Point out each Plasmodium parasite.
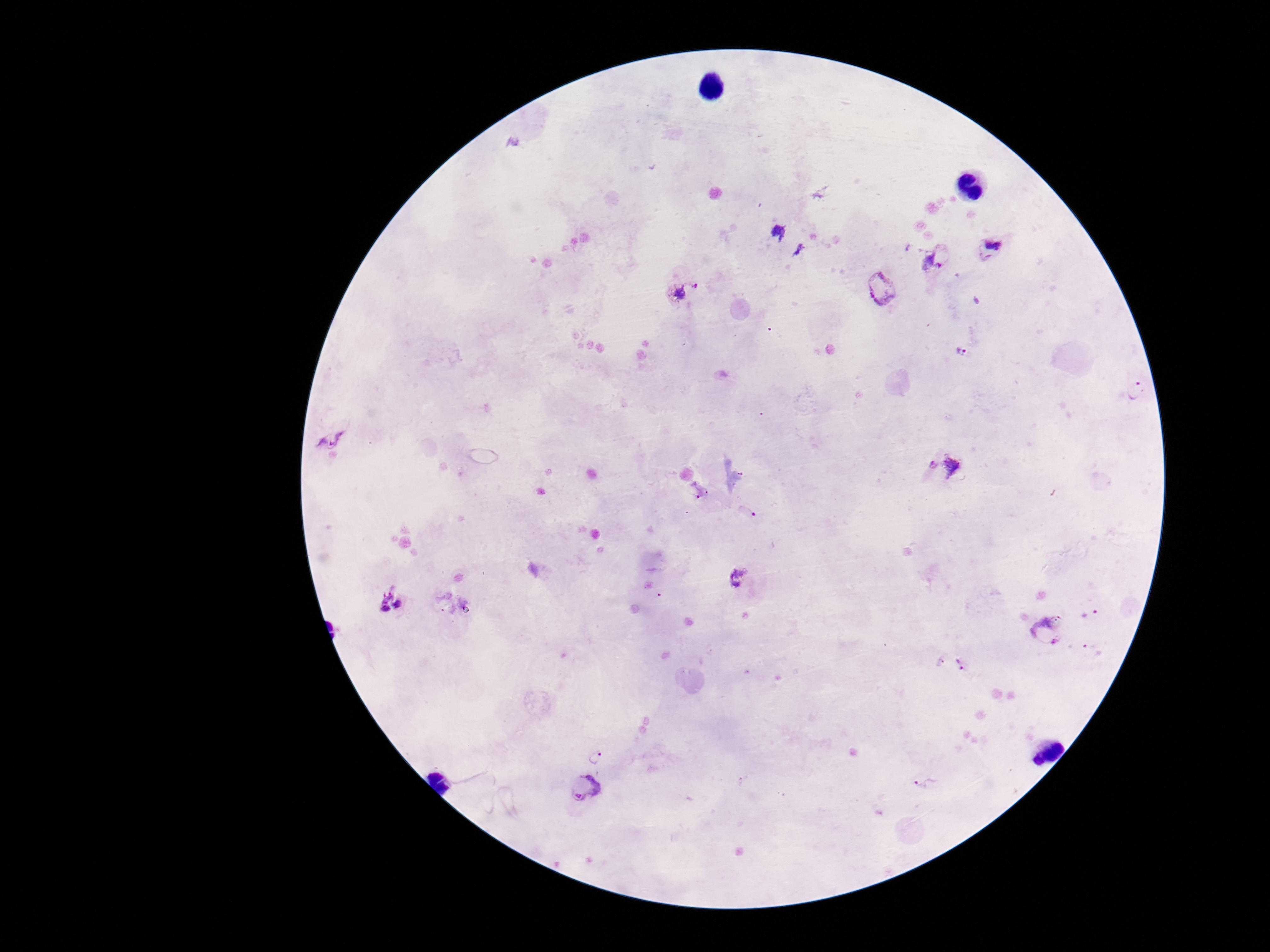

Approximate centers as {x, y} in pixels.
Plasmodium parasites: {778, 232}, {990, 250}, {934, 260}, {881, 287}, {683, 292}, {961, 351}, {1136, 391}, {330, 440}, {930, 464}, {952, 466}, {749, 510}, {738, 579}, {391, 602}, {1048, 629}, {938, 662}, {961, 663}, {596, 756}, {927, 783}, {584, 786}.

{
  "field_of_view": "single",
  "image_size": "1270×952 pixels",
  "patient_malaria_status": "infected",
  "magnification": "100x",
  "preparation": "thick blood smear",
  "stain": "Giemsa",
  "capture": "smartphone camera through the microscope eyepiece"
}